Describe the morphology of the red blood cells.
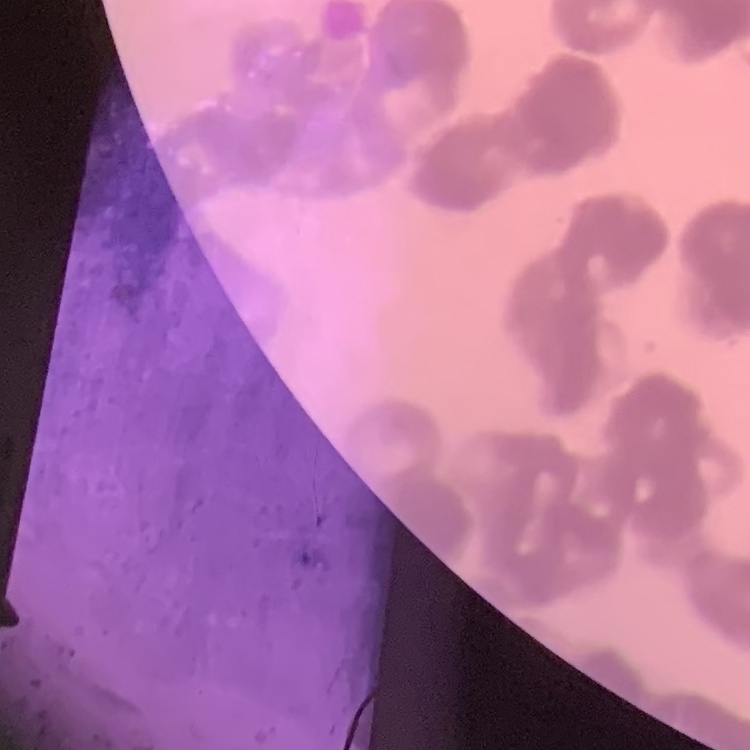

Rouleaux formation.

preparation = thin blood film
stain = Field's or Giemsa
image type = one tile cut from a larger photomicrograph